Name the blood parasite species.
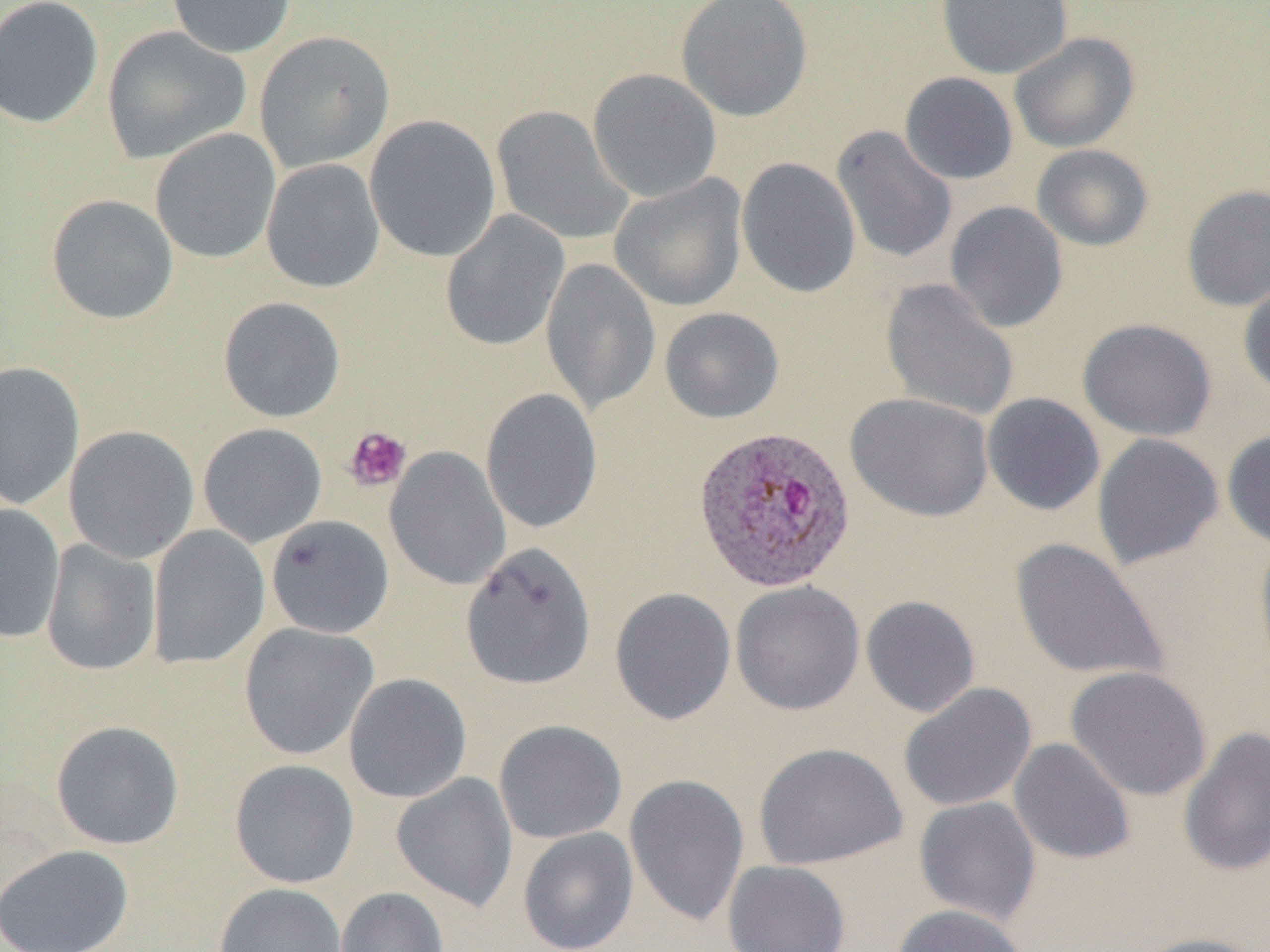

Plasmodium ovale.

{
  "uninfected_red_blood_cell_locations": "approximate bounding boxes as named x1/y1/x2/y2 corners in pixels: (x1=0, y1=0, x2=104, y2=129), (x1=167, y1=0, x2=296, y2=58), (x1=675, y1=0, x2=812, y2=121), (x1=937, y1=0, x2=1073, y2=79), (x1=101, y1=26, x2=251, y2=164), (x1=253, y1=30, x2=394, y2=172), (x1=1009, y1=31, x2=1140, y2=153), (x1=588, y1=68, x2=721, y2=201), (x1=900, y1=72, x2=1018, y2=185), (x1=492, y1=106, x2=632, y2=245), (x1=364, y1=114, x2=501, y2=262), (x1=831, y1=125, x2=958, y2=265), (x1=150, y1=128, x2=281, y2=264), (x1=1031, y1=143, x2=1154, y2=251), (x1=737, y1=157, x2=861, y2=298), (x1=261, y1=159, x2=385, y2=293), (x1=610, y1=174, x2=747, y2=311), (x1=1181, y1=184, x2=1270, y2=312), (x1=46, y1=194, x2=178, y2=324), (x1=944, y1=201, x2=1068, y2=333), (x1=440, y1=210, x2=569, y2=351), (x1=541, y1=258, x2=661, y2=416), (x1=1238, y1=274, x2=1270, y2=400), (x1=880, y1=279, x2=1020, y2=422), (x1=218, y1=296, x2=346, y2=423), (x1=659, y1=307, x2=784, y2=423), (x1=1077, y1=318, x2=1216, y2=442), (x1=0, y1=361, x2=85, y2=511), (x1=481, y1=388, x2=602, y2=535), (x1=845, y1=392, x2=994, y2=522), (x1=981, y1=392, x2=1105, y2=516), (x1=197, y1=423, x2=327, y2=548), (x1=64, y1=425, x2=199, y2=563), (x1=1222, y1=428, x2=1270, y2=551), (x1=1092, y1=433, x2=1224, y2=570), (x1=384, y1=447, x2=511, y2=591), (x1=0, y1=503, x2=65, y2=644), (x1=266, y1=515, x2=393, y2=638), (x1=147, y1=525, x2=270, y2=670), (x1=1254, y1=532, x2=1270, y2=683), (x1=1008, y1=538, x2=1169, y2=682), (x1=41, y1=540, x2=160, y2=676), (x1=461, y1=542, x2=597, y2=690), (x1=730, y1=581, x2=864, y2=716), (x1=610, y1=587, x2=736, y2=725), (x1=860, y1=595, x2=981, y2=717), (x1=238, y1=623, x2=379, y2=760), (x1=1066, y1=665, x2=1212, y2=802), (x1=344, y1=673, x2=472, y2=803), (x1=898, y1=682, x2=1037, y2=812), (x1=494, y1=719, x2=627, y2=844), (x1=50, y1=720, x2=184, y2=850), (x1=1178, y1=726, x2=1270, y2=877), (x1=1008, y1=738, x2=1136, y2=865), (x1=753, y1=742, x2=907, y2=870), (x1=229, y1=759, x2=359, y2=888), (x1=391, y1=772, x2=518, y2=913), (x1=623, y1=774, x2=750, y2=928), (x1=913, y1=796, x2=1041, y2=925), (x1=517, y1=827, x2=639, y2=952), (x1=1, y1=844, x2=133, y2=952), (x1=723, y1=860, x2=851, y2=952), (x1=214, y1=883, x2=348, y2=952), (x1=335, y1=886, x2=449, y2=952), (x1=890, y1=904, x2=1032, y2=952), (x1=1130, y1=932, x2=1267, y2=952)",
  "preparation": "thin blood film",
  "modality": "optical microscopy",
  "platelet_locations": "approximate bounding boxes as named x1/y1/x2/y2 corners in pixels: (x1=343, y1=426, x2=411, y2=492)",
  "plasmodium_ovale_infected_red_blood_cell_locations": "approximate bounding boxes as named x1/y1/x2/y2 corners in pixels: (x1=691, y1=424, x2=857, y2=594)",
  "magnification": "1000x",
  "image_size": "1270×952 pixels",
  "field_of_view": "single"
}